Classify this cell by malaria status.
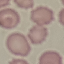
Uninfected.

Summary:
  - Preparation: thin smear
  - Image type: cell patch, automatically extracted from a larger field of view and resized to 64 × 64 pixels
  - Stain: Giemsa
  - Capture: smartphone camera at the microscope eyepiece